Assess the morphology of the erythrocytes.
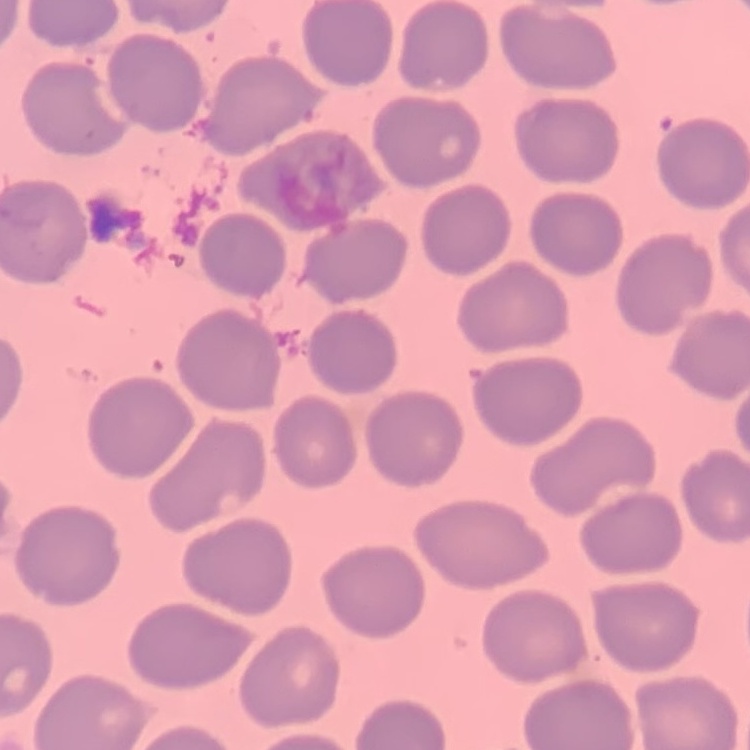
They show no rouleaux formation.

Summary:
  - Stain: Field's or Giemsa
  - Preparation: thin peripheral smear
  - Image type: one tile cut from a larger photomicrograph